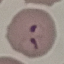

result = malaria parasites identified
image type = cell patch, automatically extracted from a larger field of view and resized to 64 × 64 pixels
preparation = thin blood film
stain = Giemsa
capture = smartphone camera at the microscope eyepiece